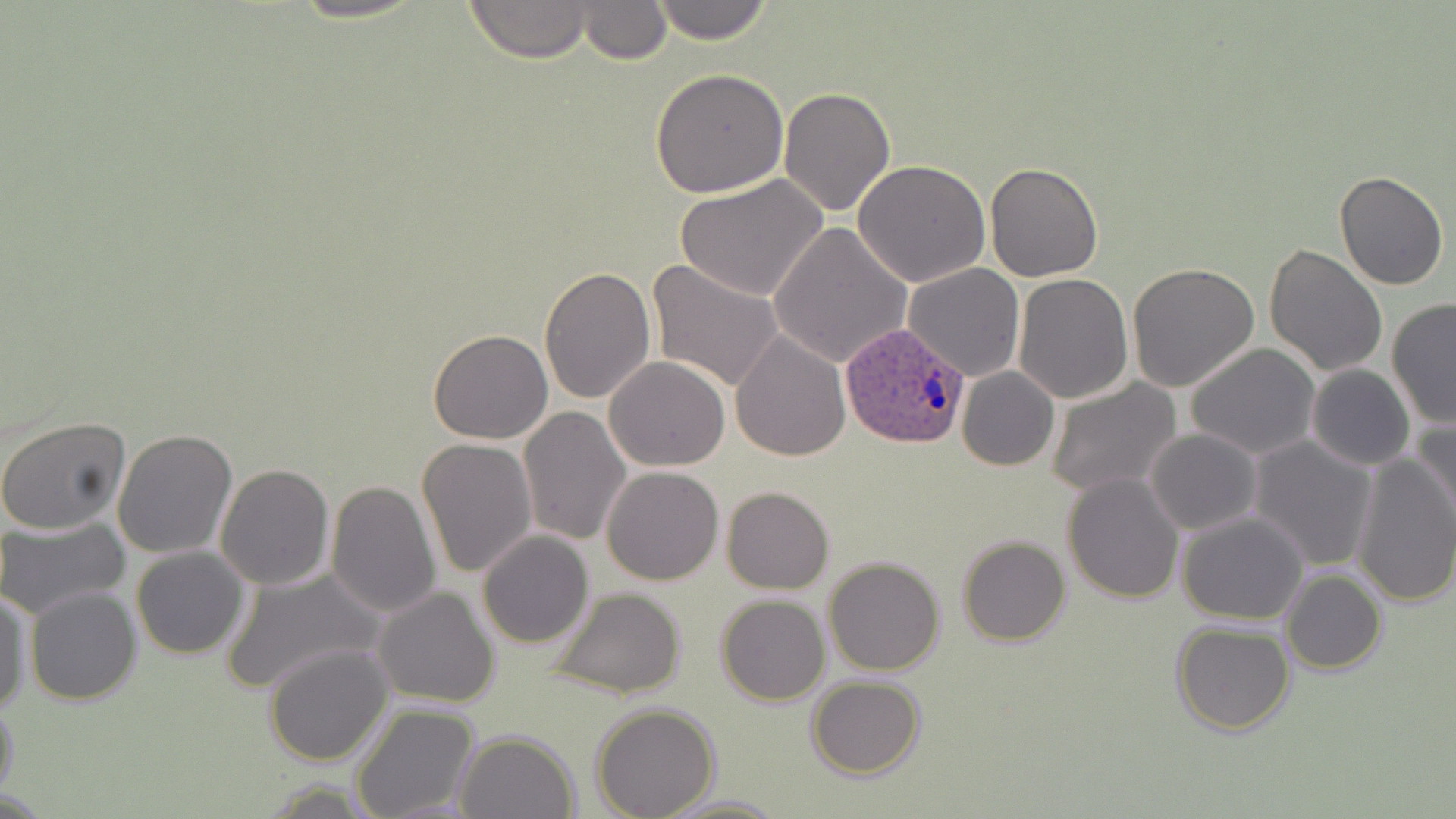

slide-level diagnosis = Plasmodium ovale
field of view = single
uninfected red blood cell locations = approximate bounding boxes as [x1, y1, x2, y2] in pixels: [461, 0, 597, 62], [648, 0, 775, 44], [578, 1, 670, 63], [649, 66, 790, 196], [778, 86, 897, 216], [852, 160, 992, 286], [984, 161, 1104, 282], [1334, 171, 1449, 291], [675, 175, 829, 302], [769, 222, 913, 366], [1263, 243, 1387, 376], [645, 258, 785, 393], [904, 263, 1024, 380], [1127, 264, 1261, 393], [539, 267, 655, 404], [1014, 273, 1133, 403], [1386, 297, 1456, 428], [427, 329, 553, 444], [731, 330, 850, 462], [1185, 343, 1320, 460], [604, 357, 731, 472], [1306, 364, 1415, 470], [957, 367, 1059, 470], [1045, 378, 1183, 497], [518, 406, 631, 545], [1410, 413, 1456, 531], [0, 415, 132, 535], [112, 428, 239, 560], [1145, 429, 1260, 536], [1249, 436, 1379, 571], [418, 437, 537, 580], [1351, 449, 1456, 607], [215, 462, 336, 591], [601, 465, 724, 586], [1062, 473, 1184, 605], [327, 480, 443, 618], [721, 487, 834, 593], [1176, 512, 1309, 625], [0, 516, 131, 619], [477, 531, 595, 648], [957, 535, 1071, 646], [130, 546, 250, 660], [823, 556, 945, 676], [218, 566, 384, 695], [1281, 569, 1386, 675], [24, 585, 141, 704], [544, 585, 689, 700], [373, 586, 501, 709], [0, 590, 33, 715], [715, 595, 830, 706], [1171, 621, 1294, 734], [263, 642, 393, 766], [807, 676, 925, 780], [0, 698, 20, 807], [350, 704, 478, 819], [590, 704, 720, 819], [454, 729, 581, 819], [662, 792, 784, 818]
stain = May-Grünwald-Giemsa
preparation = thin blood film
image size = 1456×819 pixels
modality = optical microscopy
magnification = 1000x
Plasmodium ovale-infected red blood cell locations = approximate bounding boxes as [x1, y1, x2, y2] in pixels: [840, 324, 972, 449]